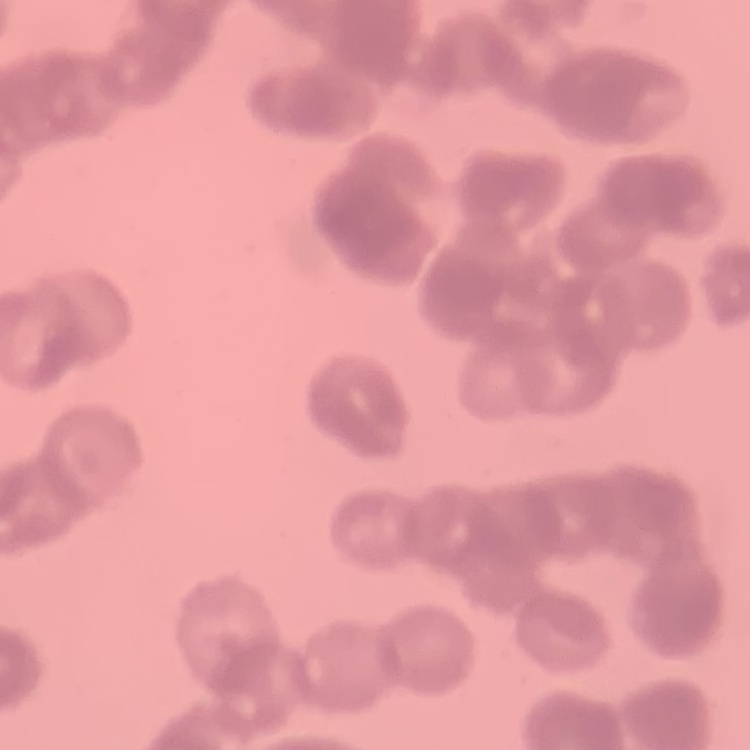
{
  "erythrocyte_morphology": "rouleaux formation",
  "image_type": "square crop of a larger photomicrograph",
  "preparation": "thin blood film",
  "stain": "Field's or Giemsa"
}